Describe the morphology of the erythrocytes.
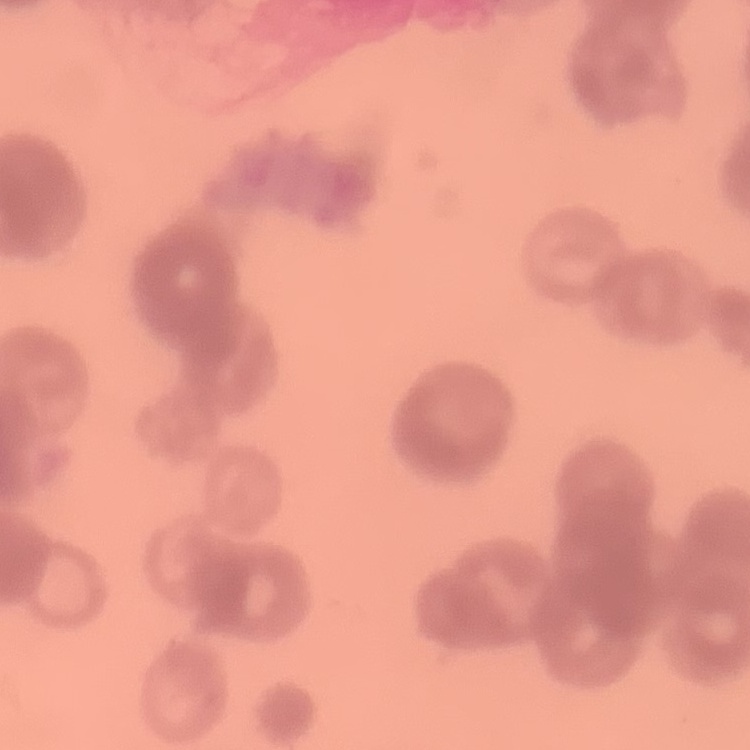

Rouleaux formation.

Summary:
  - Preparation: thin peripheral smear
  - Image type: one tile cut from a larger photomicrograph
  - Stain: Field's or Giemsa